Outline each blood parasite and name the species.
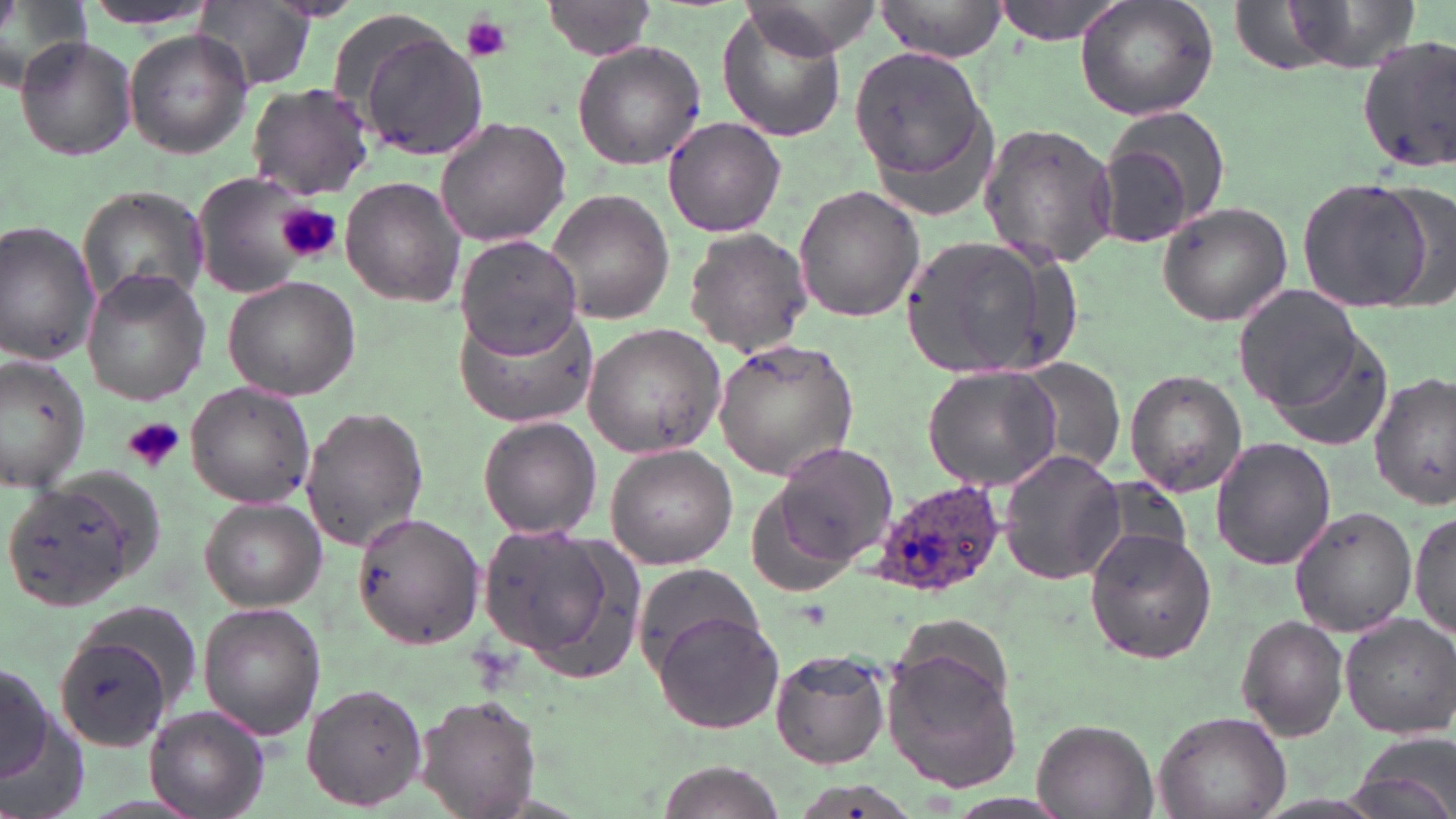

Approximate bounding boxes as (x1,y1)-(x2,y2) corner pairs in pixels.
Plasmodium ovale-infected red blood cells: (873,475)-(1010,601).
No Plasmodium falciparum, Plasmodium malariae, Plasmodium vivax, Babesia divergens, or Trypanosoma brucei observed.

Summary:
  - Platelet locations: (464,14)-(512,63), (275,204)-(341,265), (124,417)-(185,472)
  - Uninfected red blood cell locations: (0,0)-(91,94), (79,0)-(221,30), (195,0)-(315,90), (875,0)-(1010,62), (993,0)-(1132,44), (1074,0)-(1219,123), (1275,0)-(1421,75), (539,1)-(660,59), (719,6)-(845,143), (347,23)-(488,161), (123,28)-(253,159), (15,36)-(139,163), (1356,37)-(1456,174), (571,40)-(706,171), (847,45)-(993,193), (247,82)-(374,200), (1094,111)-(1227,247), (434,114)-(573,246), (663,115)-(784,237), (977,123)-(1118,267), (193,170)-(327,297), (1298,176)-(1433,312), (341,177)-(464,306), (795,184)-(925,323), (76,186)-(208,313), (548,189)-(673,324), (1158,201)-(1293,325), (0,220)-(102,366), (685,227)-(809,359), (900,232)-(1071,385), (457,234)-(583,358), (82,271)-(211,405), (223,277)-(362,401), (1235,286)-(1366,411), (458,301)-(592,425), (583,322)-(726,460), (713,340)-(859,480), (0,352)-(94,488), (1017,360)-(1126,479), (922,367)-(1064,493), (1124,370)-(1248,499), (1370,372)-(1454,511), (185,382)-(315,509), (300,405)-(428,552), (478,414)-(599,538), (1211,437)-(1337,571), (770,441)-(898,565), (606,443)-(738,569), (998,450)-(1126,585), (1097,478)-(1193,570), (5,481)-(142,610), (198,497)-(328,613), (1289,504)-(1419,636), (352,509)-(485,650), (1410,509)-(1455,643), (471,523)-(616,666), (1086,529)-(1217,664), (635,566)-(768,667), (198,601)-(326,739), (651,609)-(787,733), (1340,614)-(1455,739), (1237,616)-(1348,739), (53,627)-(182,755), (770,650)-(890,769), (0,653)-(61,803), (882,654)-(1024,790), (301,682)-(428,811), (417,695)-(542,819), (144,706)-(268,817), (1154,709)-(1290,819), (1031,718)-(1157,818), (1353,734)-(1456,819), (653,762)-(781,819)
  - Slide-level diagnosis: Plasmodium ovale
  - Preparation: thin blood smear
  - Magnification: 1000x
  - Field of view: one of a larger specimen
  - Stain: May-Grünwald-Giemsa
  - Modality: light microscopy
  - Image size: 1456×819 pixels